Outline each blood parasite and name the species.
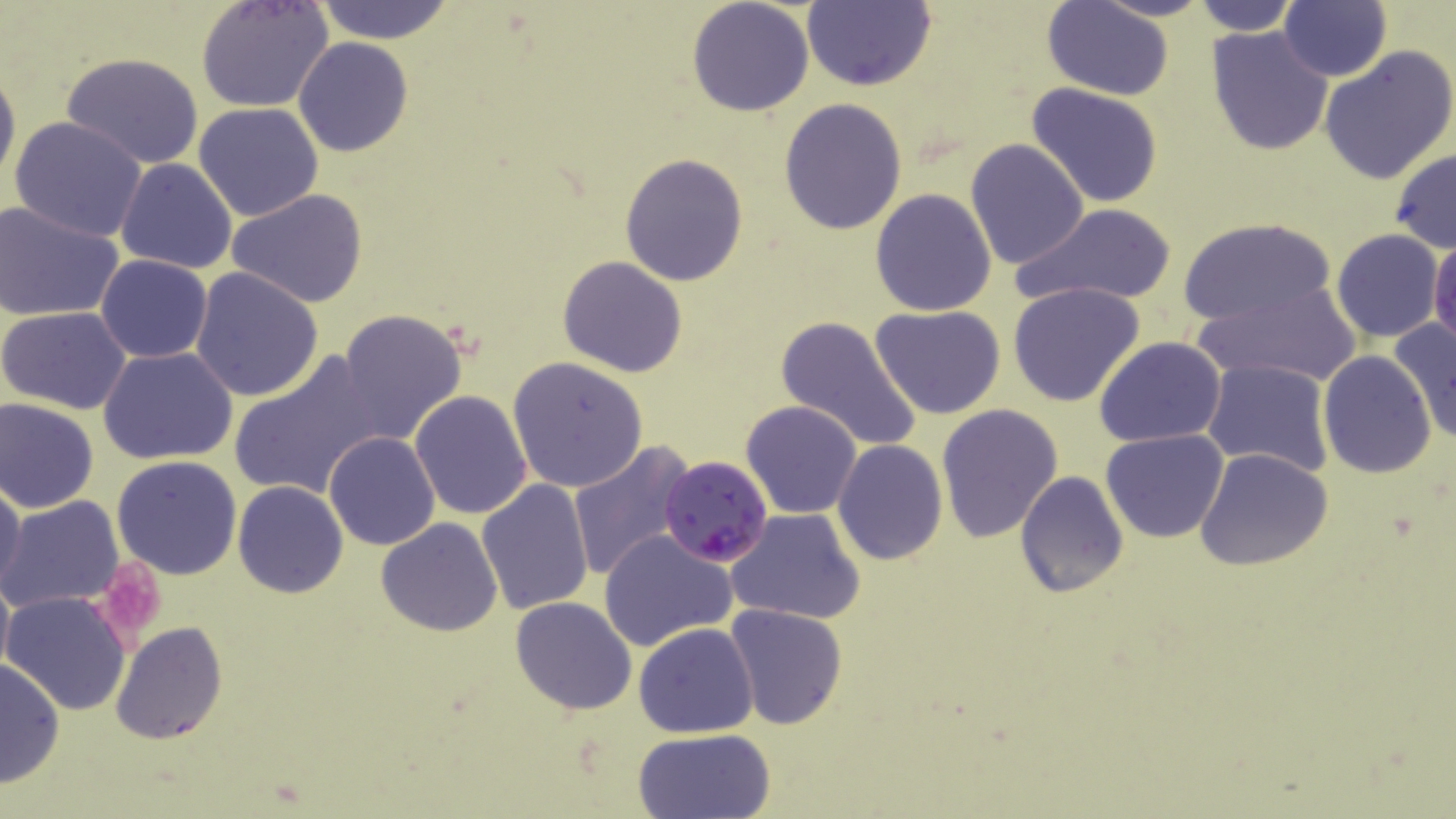
Approximate bounding boxes as named x1/y1/x2/y2 corners in pixels.
Plasmodium falciparum-infected red blood cells: (x1=660, y1=456, x2=774, y2=568).
No Plasmodium ovale, Plasmodium malariae, Plasmodium vivax, Babesia divergens, or Trypanosoma brucei observed.

slide-level diagnosis = Plasmodium falciparum
preparation = thin blood film
uninfected red blood cell locations = approximate bounding boxes as named x1/y1/x2/y2 corners in pixels: (x1=311, y1=0, x2=457, y2=43), (x1=1088, y1=0, x2=1215, y2=22), (x1=1187, y1=0, x2=1302, y2=36), (x1=1279, y1=0, x2=1391, y2=82), (x1=196, y1=1, x2=334, y2=112), (x1=686, y1=1, x2=815, y2=117), (x1=803, y1=1, x2=934, y2=91), (x1=1044, y1=2, x2=1173, y2=99), (x1=1205, y1=27, x2=1334, y2=155), (x1=293, y1=37, x2=414, y2=156), (x1=1320, y1=43, x2=1456, y2=185), (x1=59, y1=53, x2=206, y2=169), (x1=0, y1=60, x2=20, y2=197), (x1=1026, y1=84, x2=1165, y2=208), (x1=779, y1=97, x2=909, y2=235), (x1=193, y1=102, x2=325, y2=221), (x1=8, y1=116, x2=150, y2=243), (x1=965, y1=139, x2=1088, y2=269), (x1=1389, y1=147, x2=1456, y2=254), (x1=618, y1=153, x2=749, y2=286), (x1=115, y1=158, x2=237, y2=274), (x1=870, y1=188, x2=998, y2=316), (x1=226, y1=189, x2=370, y2=310), (x1=0, y1=199, x2=124, y2=323), (x1=1013, y1=202, x2=1178, y2=308), (x1=1179, y1=217, x2=1336, y2=329), (x1=1331, y1=230, x2=1444, y2=343), (x1=1430, y1=232, x2=1456, y2=354), (x1=95, y1=254, x2=213, y2=364), (x1=557, y1=255, x2=689, y2=377), (x1=189, y1=265, x2=324, y2=401), (x1=1009, y1=281, x2=1147, y2=407), (x1=1191, y1=284, x2=1365, y2=389), (x1=870, y1=305, x2=1007, y2=419), (x1=0, y1=307, x2=132, y2=414), (x1=336, y1=310, x2=470, y2=447), (x1=777, y1=314, x2=920, y2=452), (x1=1388, y1=317, x2=1456, y2=446), (x1=1094, y1=337, x2=1227, y2=448), (x1=98, y1=346, x2=240, y2=464), (x1=228, y1=350, x2=385, y2=500), (x1=1318, y1=350, x2=1437, y2=479), (x1=507, y1=357, x2=648, y2=493), (x1=1203, y1=359, x2=1335, y2=477), (x1=408, y1=391, x2=531, y2=519), (x1=0, y1=398, x2=99, y2=512), (x1=740, y1=401, x2=863, y2=519), (x1=935, y1=404, x2=1064, y2=544), (x1=1102, y1=429, x2=1229, y2=543), (x1=323, y1=431, x2=442, y2=550), (x1=568, y1=440, x2=695, y2=579), (x1=833, y1=440, x2=948, y2=565), (x1=1195, y1=448, x2=1333, y2=571), (x1=111, y1=454, x2=242, y2=579), (x1=1014, y1=470, x2=1129, y2=598), (x1=0, y1=476, x2=24, y2=596), (x1=477, y1=479, x2=595, y2=615), (x1=233, y1=481, x2=348, y2=598), (x1=1, y1=495, x2=127, y2=614), (x1=727, y1=508, x2=867, y2=625), (x1=378, y1=517, x2=502, y2=636), (x1=598, y1=529, x2=736, y2=651), (x1=0, y1=570, x2=14, y2=683), (x1=3, y1=591, x2=133, y2=716), (x1=510, y1=596, x2=638, y2=715), (x1=725, y1=603, x2=847, y2=729), (x1=112, y1=621, x2=227, y2=744), (x1=633, y1=621, x2=760, y2=736), (x1=0, y1=656, x2=64, y2=790), (x1=631, y1=729, x2=775, y2=818)
image size = 1456×819 pixels
stain = May-Grünwald-Giemsa
field of view = single
modality = light microscopy
magnification = 1000x